Report the malaria status of this cell.
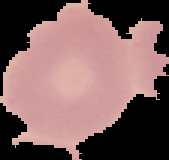
It is uninfected.

Image is 169×160 pixels. From a thin blood smear. The area outside the segmented cell region is set to black.